Give the extent of the malaria parasites you find, grouped by life-cycle stage — ring form, trophozoite, schizont, or gametocyte.
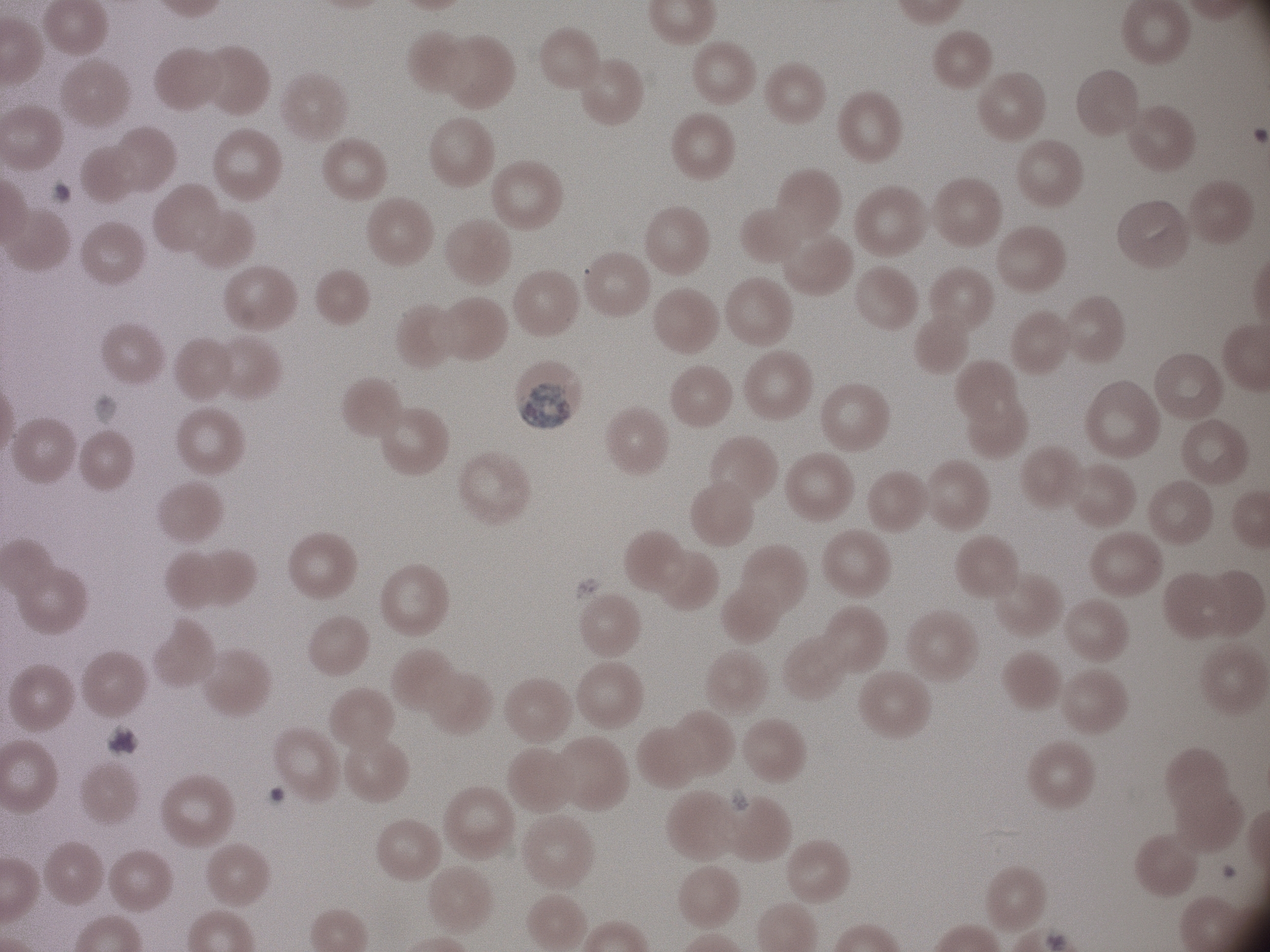
Approximate bounding boxes as (x1, y1, x2, y2) in pixels, from the source annotation, which is not necessarily exhaustive.
Gametocytes: (516, 382, 574, 429).

magnification = 100x
field of view = single
species = Plasmodium malariae
image size = 1270×952 pixels
preparation = thin blood smear
microscope = Leica DM2000 with built-in camera
stain = Giemsa